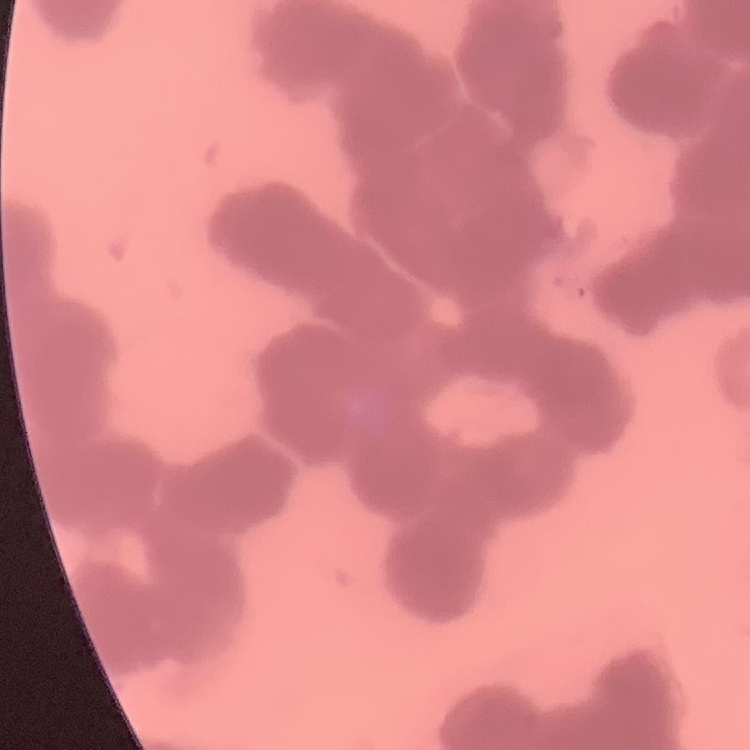

Summary:
  - Erythrocyte morphology: rouleaux formation
  - Stain: Field's or Giemsa
  - Preparation: thin blood film
  - Image type: one tile cut from a larger photomicrograph